Identify the cell.
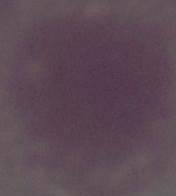

An erythrocyte.

Summary:
  - Magnification: 1000x
  - Modality: micrograph